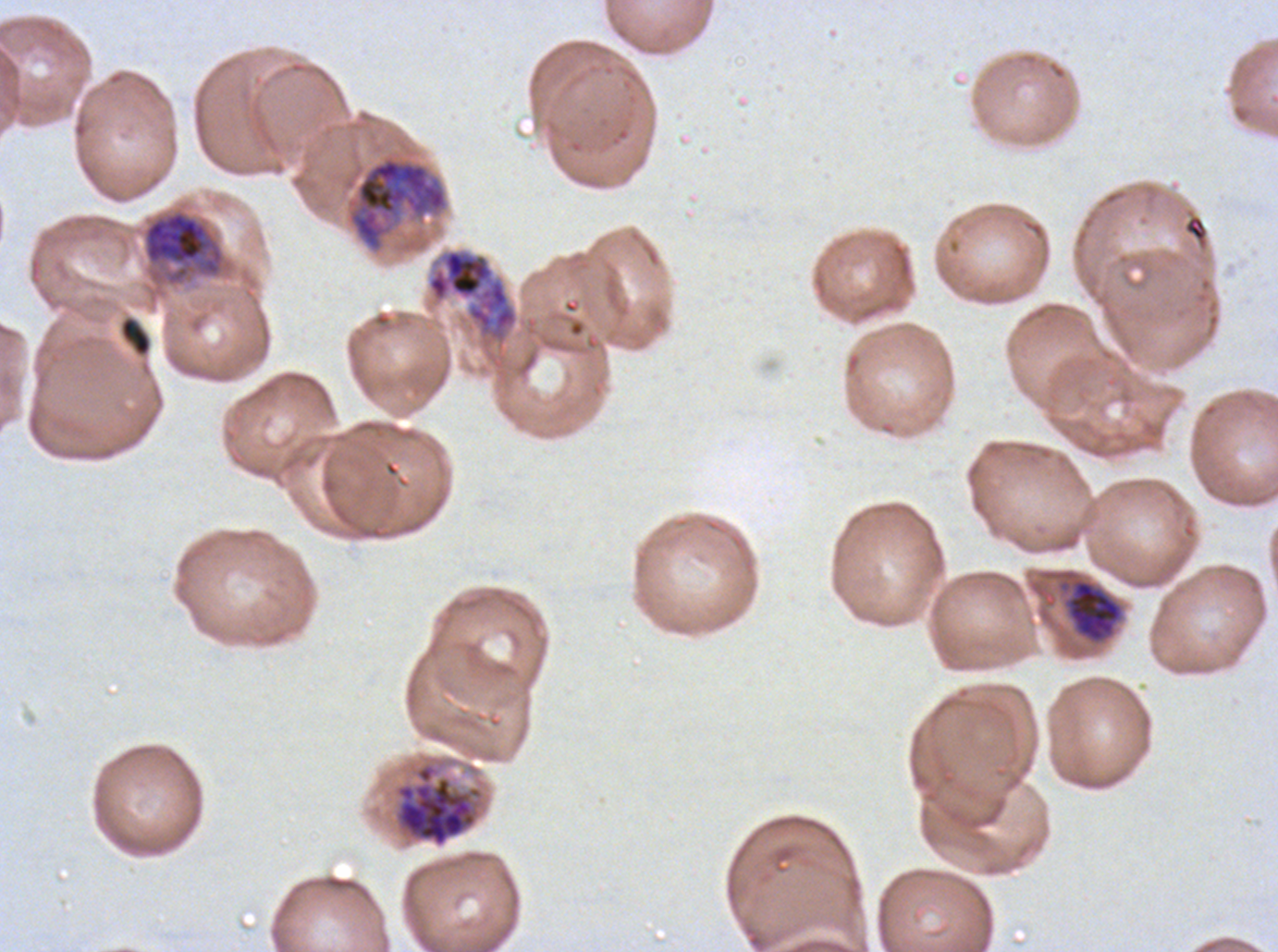

notation = approximate bounding boxes as [x1, y1, x2, y2] in pixels
late schizont locations = [385, 753, 490, 849]
late trophozoite locations = [1064, 578, 1124, 643]
debris locations = [118, 314, 153, 358]
early schizont locations = [347, 155, 449, 252], [141, 208, 227, 287], [426, 248, 519, 347]
image size = 1278×952 pixels
preparation = thin blood film
field of view = sub-image separated from a larger composite
life-cycle stages observed = late trophozoite, early schizont, late schizont
specimen = Plasmodium falciparum cultured ex vivo for 24 to 48 hours, from a patient in The Gambia
stain = Giemsa